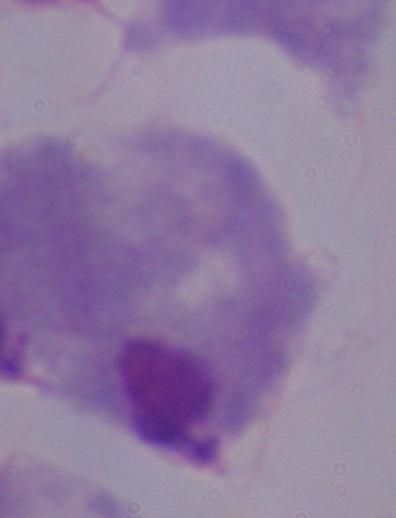 1000x magnification. Photomicrograph. A trichomonad is seen.